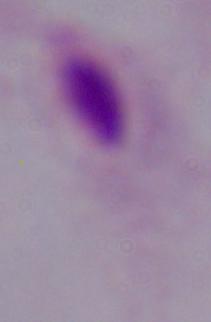
modality = micrograph
magnification = 1000x
identification = trichomonad